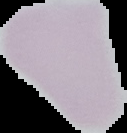
{
  "malaria_status": "uninfected",
  "image_size": "127×133 pixels",
  "preparation": "thin blood smear",
  "image_type": "segmented cell region with the area outside set to black"
}